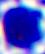 A white blood cell is seen. Micrograph. 400x magnification.